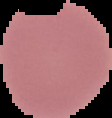
Summary:
  - Preparation: thin blood smear
  - Malaria status: uninfected
  - Image size: 112×118 pixels
  - Image type: segmented cell region with the area outside set to black